Assess this cell for malaria.
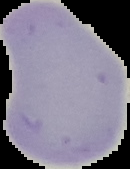
It is uninfected.

preparation = thin blood smear
image size = 130×169 pixels
image type = cell region segmented out of the field of view; surrounding area masked to black